Outline every leukocyte.
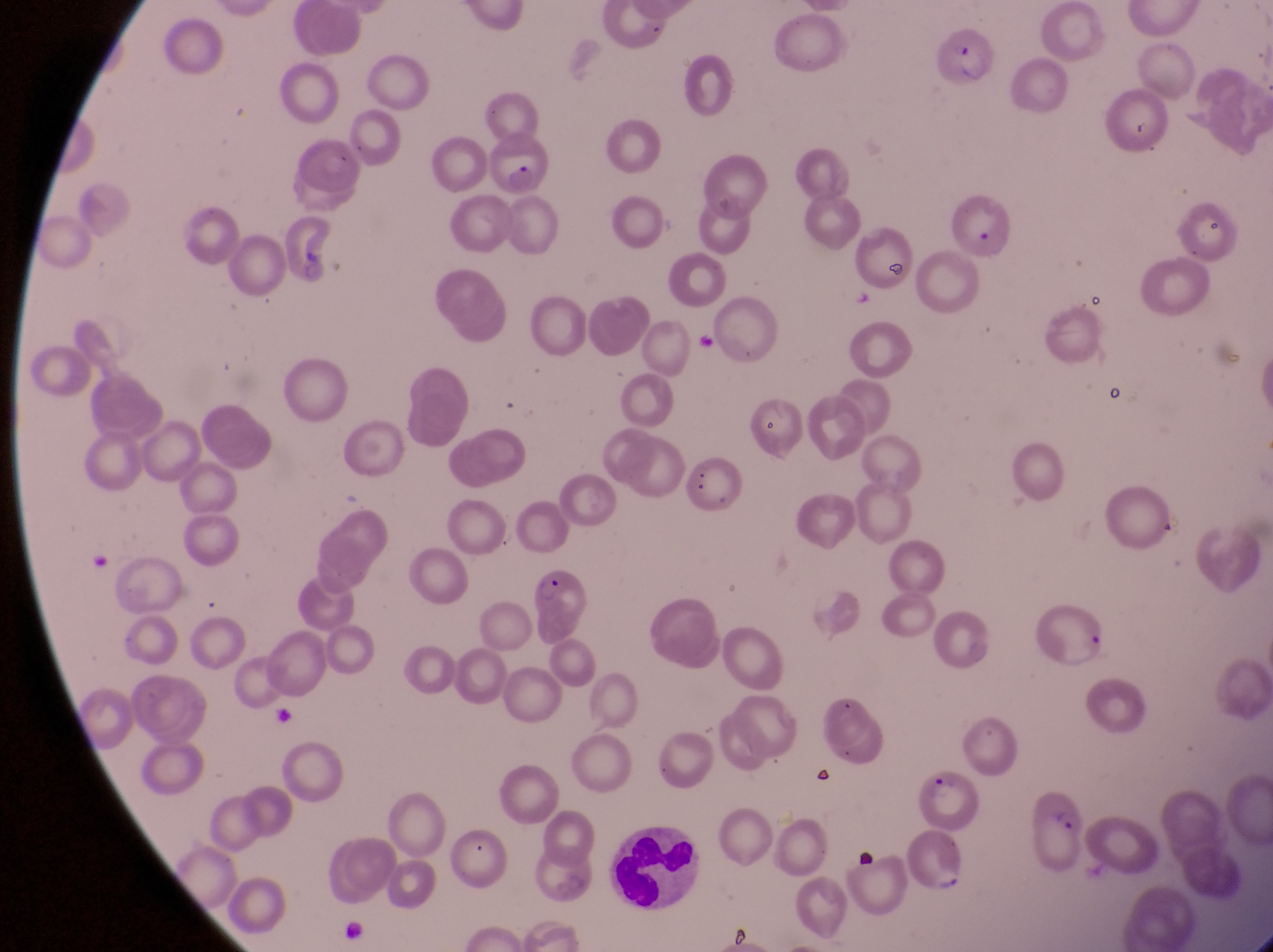

Approximate bounding boxes as {left, top, right, bottom} in pixels.
Leukocytes: {612, 829, 714, 909}.

Parasitised red blood cell locations: {934, 23, 997, 88}, {487, 130, 552, 195}, {744, 397, 807, 460}, {519, 569, 584, 627}, {917, 772, 982, 827}, {1021, 796, 1090, 870}, {903, 832, 972, 902}. Captured by a smartphone held over the eyepiece of an Olympus CX-23 microscope. Image is 1273×952 pixels. Sample from Uganda. Thin blood film. Magnification of 1000x. One field of view.